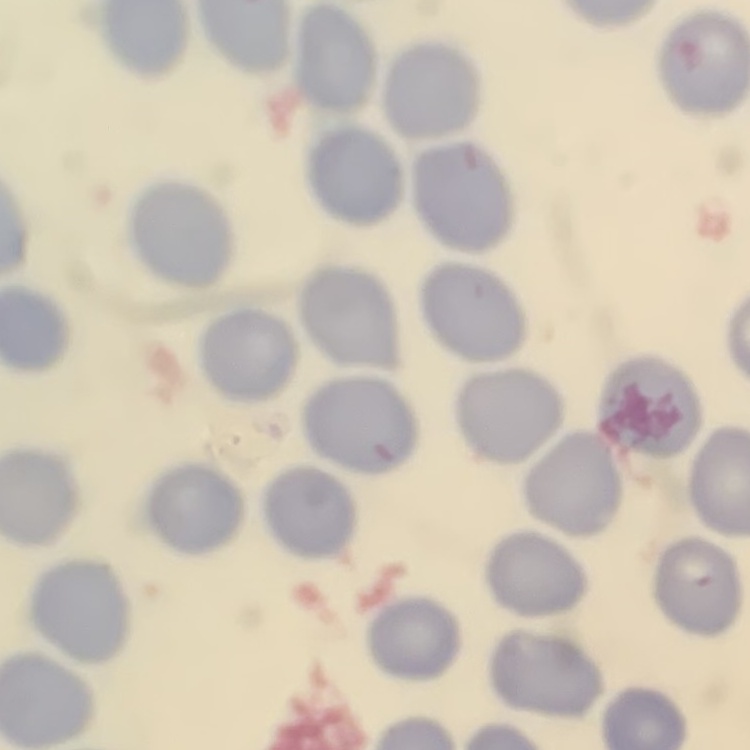
Summary:
  - Erythrocyte morphology: no rouleaux formation
  - Image type: square crop of a larger photomicrograph
  - Stain: Field's or Giemsa
  - Preparation: thin blood film